Name the parasite shown.
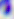
Toxoplasma gondii.

{
  "magnification": "400x",
  "modality": "photomicrograph"
}